State the blood parasite species.
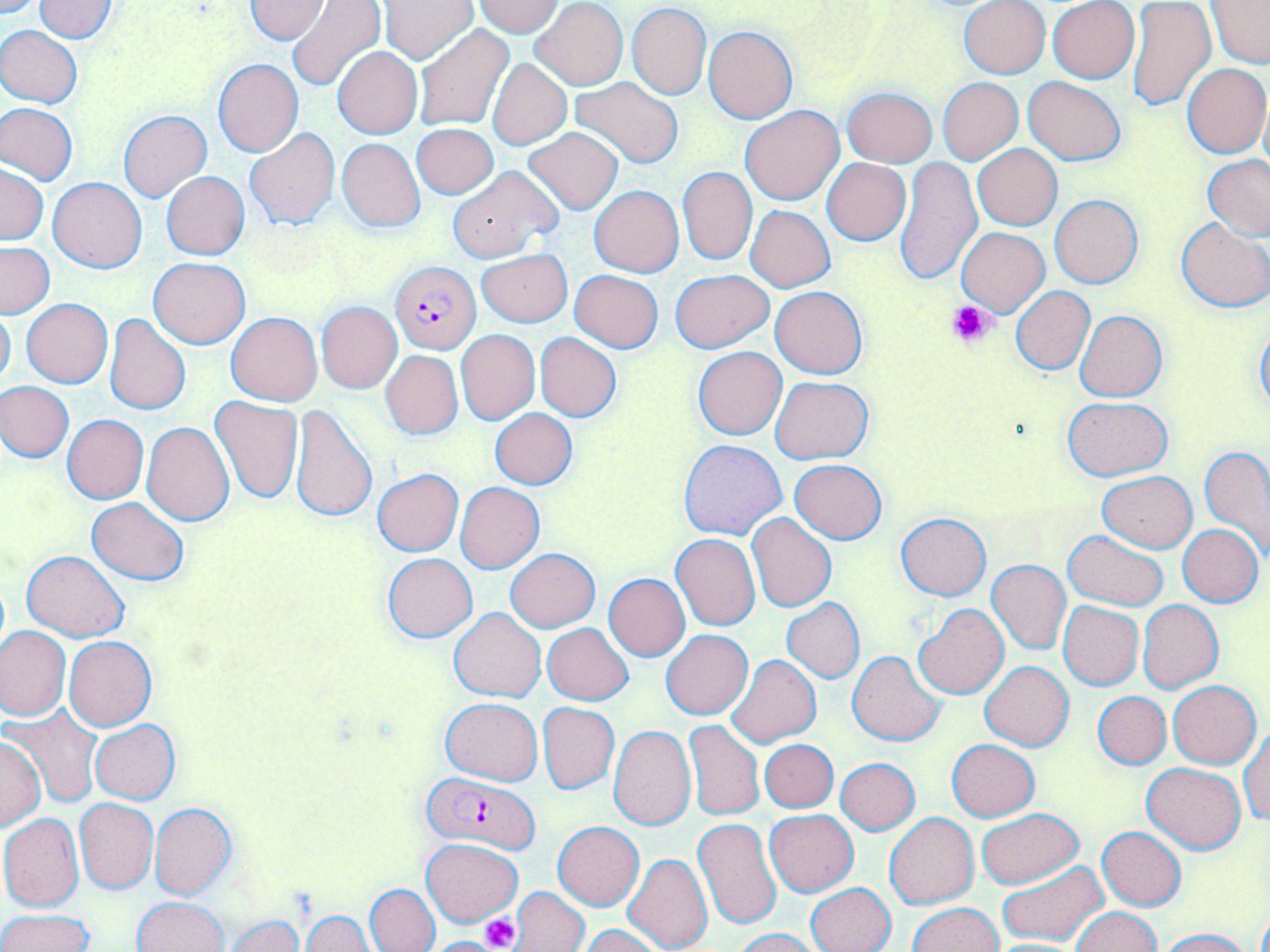
Plasmodium falciparum.

Approximate bounding boxes as named x1/y1/x2/y2 corners in pixels. Platelet locations: (x1=945, y1=298, x2=997, y2=350), (x1=479, y1=913, x2=521, y2=951). Uninfected red blood cell locations: (x1=245, y1=0, x2=330, y2=42), (x1=33, y1=1, x2=121, y2=41), (x1=288, y1=1, x2=388, y2=91), (x1=379, y1=1, x2=478, y2=64), (x1=474, y1=1, x2=565, y2=36), (x1=958, y1=1, x2=1050, y2=79), (x1=1047, y1=1, x2=1140, y2=84), (x1=530, y1=2, x2=628, y2=89), (x1=1127, y1=2, x2=1215, y2=112), (x1=1205, y1=2, x2=1270, y2=68), (x1=626, y1=3, x2=711, y2=99), (x1=0, y1=25, x2=84, y2=108), (x1=413, y1=25, x2=515, y2=133), (x1=703, y1=25, x2=797, y2=124), (x1=332, y1=46, x2=423, y2=138), (x1=487, y1=58, x2=571, y2=150), (x1=212, y1=59, x2=304, y2=156), (x1=1183, y1=63, x2=1269, y2=159), (x1=1023, y1=75, x2=1125, y2=166), (x1=569, y1=76, x2=684, y2=169), (x1=938, y1=77, x2=1023, y2=165), (x1=841, y1=86, x2=938, y2=166), (x1=1, y1=102, x2=77, y2=185), (x1=740, y1=105, x2=844, y2=205), (x1=119, y1=111, x2=212, y2=201), (x1=412, y1=123, x2=498, y2=199), (x1=523, y1=127, x2=623, y2=215), (x1=244, y1=128, x2=340, y2=230), (x1=336, y1=138, x2=426, y2=233), (x1=974, y1=144, x2=1062, y2=230), (x1=1202, y1=154, x2=1270, y2=240), (x1=896, y1=157, x2=982, y2=286), (x1=822, y1=158, x2=911, y2=246), (x1=0, y1=165, x2=48, y2=244), (x1=447, y1=166, x2=561, y2=264), (x1=677, y1=167, x2=758, y2=267), (x1=161, y1=172, x2=249, y2=260), (x1=48, y1=177, x2=147, y2=273), (x1=589, y1=185, x2=685, y2=278), (x1=1050, y1=194, x2=1143, y2=288), (x1=746, y1=206, x2=835, y2=291), (x1=1176, y1=218, x2=1270, y2=313), (x1=957, y1=228, x2=1049, y2=316), (x1=1, y1=243, x2=54, y2=318), (x1=476, y1=249, x2=572, y2=326), (x1=148, y1=258, x2=250, y2=348), (x1=671, y1=269, x2=774, y2=353), (x1=569, y1=270, x2=663, y2=352), (x1=770, y1=286, x2=869, y2=380), (x1=1011, y1=286, x2=1095, y2=375), (x1=22, y1=298, x2=113, y2=388), (x1=316, y1=302, x2=401, y2=393), (x1=0, y1=303, x2=16, y2=393), (x1=1074, y1=309, x2=1167, y2=402), (x1=104, y1=313, x2=191, y2=415), (x1=227, y1=313, x2=322, y2=406), (x1=1255, y1=320, x2=1270, y2=414), (x1=456, y1=330, x2=540, y2=425), (x1=535, y1=333, x2=621, y2=421), (x1=692, y1=347, x2=787, y2=440), (x1=380, y1=350, x2=464, y2=440), (x1=770, y1=376, x2=873, y2=464), (x1=2, y1=381, x2=74, y2=462), (x1=210, y1=396, x2=304, y2=504), (x1=1062, y1=397, x2=1173, y2=481), (x1=288, y1=405, x2=378, y2=523), (x1=490, y1=408, x2=578, y2=490), (x1=62, y1=415, x2=149, y2=504), (x1=142, y1=422, x2=235, y2=526), (x1=678, y1=438, x2=787, y2=540), (x1=1201, y1=447, x2=1270, y2=561), (x1=789, y1=459, x2=887, y2=545), (x1=372, y1=467, x2=464, y2=557), (x1=1097, y1=470, x2=1197, y2=553), (x1=455, y1=482, x2=545, y2=573), (x1=86, y1=498, x2=190, y2=584), (x1=896, y1=512, x2=990, y2=601), (x1=746, y1=513, x2=837, y2=613), (x1=1177, y1=524, x2=1263, y2=607), (x1=1062, y1=530, x2=1169, y2=610), (x1=671, y1=534, x2=761, y2=631), (x1=506, y1=549, x2=600, y2=632), (x1=23, y1=550, x2=128, y2=642), (x1=382, y1=553, x2=477, y2=644), (x1=986, y1=560, x2=1070, y2=656), (x1=603, y1=574, x2=690, y2=661), (x1=782, y1=598, x2=864, y2=684), (x1=1137, y1=600, x2=1223, y2=693), (x1=1058, y1=601, x2=1143, y2=690), (x1=913, y1=604, x2=1009, y2=698), (x1=449, y1=608, x2=546, y2=702), (x1=542, y1=623, x2=633, y2=705), (x1=1, y1=625, x2=71, y2=720), (x1=661, y1=629, x2=752, y2=720), (x1=65, y1=636, x2=156, y2=732), (x1=847, y1=650, x2=948, y2=745), (x1=724, y1=653, x2=821, y2=748), (x1=980, y1=660, x2=1074, y2=752), (x1=1166, y1=680, x2=1261, y2=768), (x1=1093, y1=691, x2=1170, y2=769), (x1=440, y1=697, x2=543, y2=784), (x1=538, y1=702, x2=619, y2=794), (x1=4, y1=705, x2=103, y2=806), (x1=89, y1=720, x2=181, y2=804), (x1=684, y1=720, x2=764, y2=822), (x1=608, y1=724, x2=697, y2=831), (x1=1239, y1=725, x2=1269, y2=827), (x1=0, y1=735, x2=45, y2=830), (x1=760, y1=739, x2=838, y2=813), (x1=946, y1=739, x2=1040, y2=821), (x1=836, y1=757, x2=920, y2=835), (x1=1142, y1=762, x2=1246, y2=854), (x1=74, y1=798, x2=158, y2=893), (x1=150, y1=804, x2=238, y2=901), (x1=976, y1=808, x2=1082, y2=888), (x1=765, y1=810, x2=858, y2=896), (x1=1, y1=813, x2=85, y2=911), (x1=883, y1=813, x2=979, y2=909), (x1=693, y1=818, x2=782, y2=933), (x1=553, y1=821, x2=644, y2=911), (x1=1096, y1=827, x2=1186, y2=911), (x1=420, y1=838, x2=523, y2=927), (x1=623, y1=854, x2=713, y2=952), (x1=998, y1=860, x2=1110, y2=947), (x1=805, y1=882, x2=896, y2=951), (x1=365, y1=883, x2=440, y2=952), (x1=510, y1=886, x2=591, y2=951), (x1=135, y1=897, x2=229, y2=952), (x1=906, y1=902, x2=1003, y2=952), (x1=1072, y1=907, x2=1159, y2=952), (x1=1, y1=908, x2=95, y2=952), (x1=301, y1=911, x2=375, y2=951), (x1=225, y1=914, x2=304, y2=952), (x1=580, y1=924, x2=666, y2=952), (x1=733, y1=928, x2=820, y2=951), (x1=1158, y1=928, x2=1251, y2=951), (x1=984, y1=939, x2=1088, y2=951). Plasmodium falciparum-infected red blood cell locations: (x1=390, y1=261, x2=480, y2=355), (x1=424, y1=771, x2=540, y2=856). Light microscopy. May-Grünwald-Giemsa-stained preparation. Image is 1270×952 pixels. Captured at 1000x magnification. Single field of view. Thin blood smear.